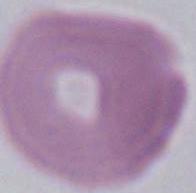

Micrograph. 1000x magnification. A red blood cell is seen.